Name the parasite shown.
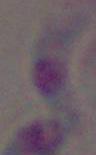

Toxoplasma gondii.

Summary:
  - Modality: micrograph
  - Magnification: 1000x